Comment on the morphology of the red blood cells.
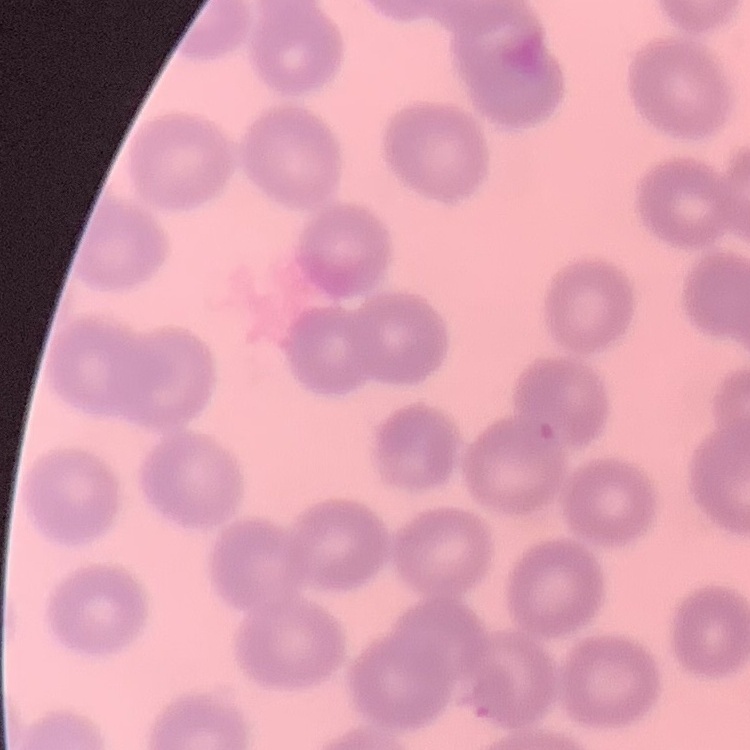

They show no rouleaux formation.

Summary:
  - Preparation: thin peripheral smear
  - Stain: Field's or Giemsa
  - Image type: square crop of a larger photomicrograph